Name the blood parasite species.
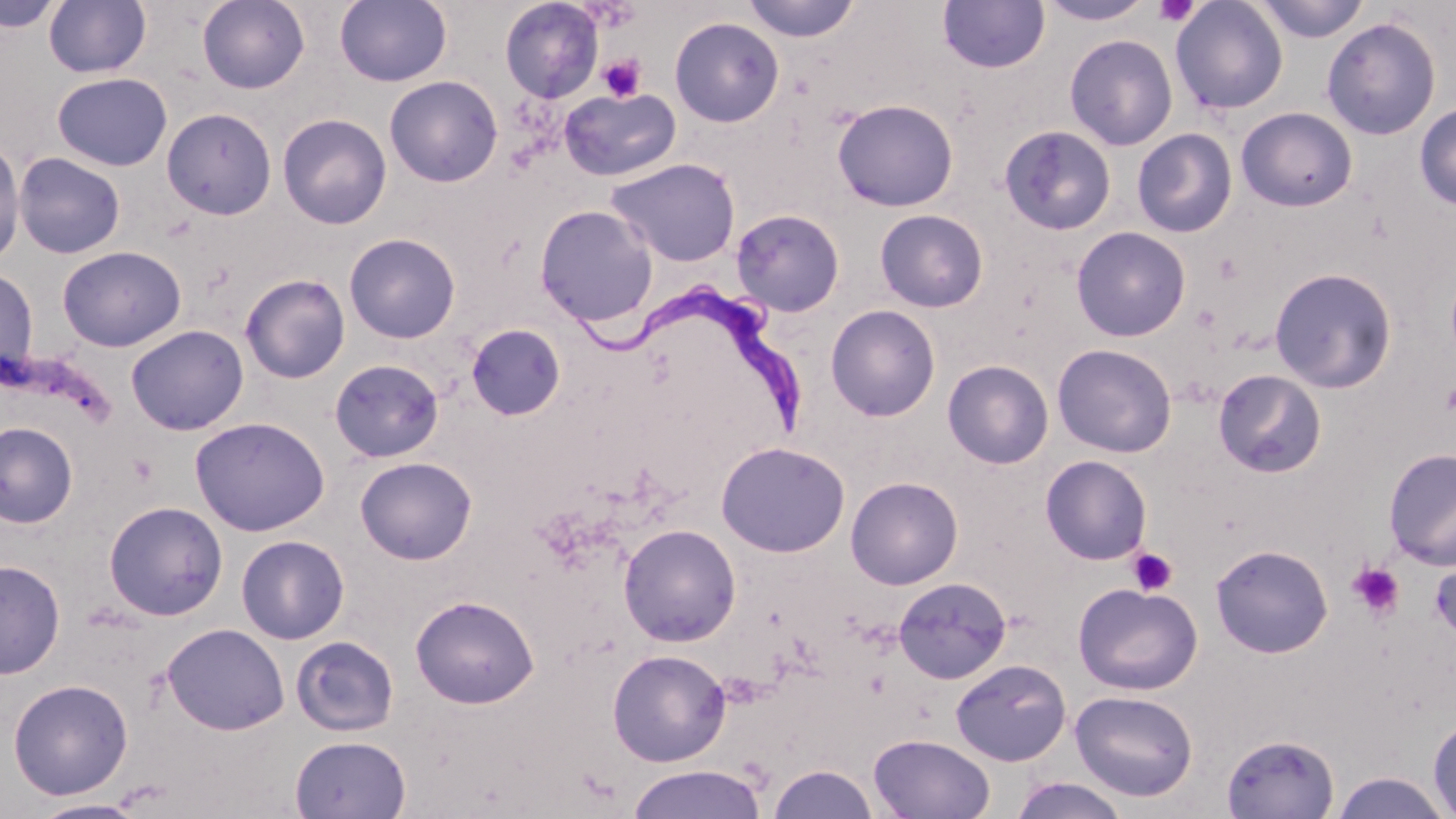
Trypanosoma brucei.

magnification = 1000x
stain = May-Grünwald-Giemsa
preparation = thin blood film
Trypanosoma brucei locations = approximate bounding boxes as [x1, y1, x2, y2] in pixels: [572, 286, 810, 430]
modality = optical microscopy
platelet locations = approximate bounding boxes as [x1, y1, x2, y2] in pixels: [1153, 1, 1200, 26], [583, 2, 640, 32], [599, 54, 646, 102], [1126, 547, 1177, 596], [1346, 562, 1405, 620]
uninfected red blood cell locations = approximate bounding boxes as [x1, y1, x2, y2] in pixels: [0, 0, 64, 33], [197, 0, 310, 94], [335, 0, 452, 87], [500, 0, 603, 103], [741, 0, 860, 42], [937, 0, 1050, 74], [1036, 0, 1155, 25], [1251, 0, 1371, 43], [43, 1, 151, 78], [1170, 1, 1289, 116], [669, 17, 784, 127], [1321, 17, 1441, 140], [1064, 34, 1178, 151], [53, 73, 172, 171], [384, 75, 503, 187], [559, 88, 681, 181], [832, 99, 958, 211], [1414, 103, 1456, 211], [1236, 107, 1358, 212], [161, 108, 277, 220], [277, 113, 391, 229], [999, 124, 1117, 236], [1132, 128, 1238, 238], [0, 136, 26, 267], [13, 152, 125, 259], [606, 157, 740, 267], [534, 205, 659, 328], [731, 208, 845, 317], [874, 209, 989, 312], [1070, 226, 1191, 342], [344, 232, 461, 344], [57, 246, 186, 352], [0, 267, 38, 383], [1269, 267, 1397, 393], [240, 273, 351, 384], [825, 304, 941, 422], [125, 324, 249, 435], [466, 324, 565, 420], [1052, 343, 1177, 457], [329, 359, 444, 462], [942, 359, 1054, 469], [1213, 369, 1326, 479], [190, 416, 330, 536], [0, 421, 78, 529], [715, 441, 850, 558], [1383, 448, 1456, 570], [1040, 455, 1152, 565], [355, 457, 477, 564], [845, 476, 963, 589], [103, 501, 229, 621], [618, 523, 741, 647], [236, 534, 350, 644], [1210, 544, 1333, 658], [1431, 555, 1456, 645], [0, 559, 65, 679], [892, 576, 1012, 684], [1073, 582, 1203, 695], [410, 594, 539, 709], [162, 623, 289, 735], [290, 635, 399, 737], [607, 648, 731, 766], [950, 659, 1071, 766], [7, 678, 133, 800], [1070, 690, 1199, 801], [1428, 716, 1456, 816], [868, 733, 995, 818], [1221, 733, 1339, 818], [289, 734, 412, 819], [627, 764, 767, 819], [768, 764, 879, 819], [1328, 771, 1454, 818], [1007, 777, 1132, 818], [28, 799, 148, 819]
image size = 1456×819 pixels
field of view = single